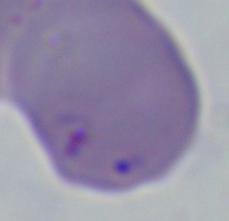

Micrograph. Captured at 1000x magnification. A Babesia parasite is shown.